Assess this cell for malaria.
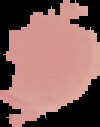
Uninfected.

From a thin blood smear. Image is 100×127 pixels. Cell region segmented out of the field of view; the surrounding area is masked to black.